Assess this cell for malaria.
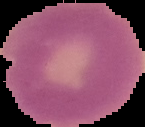
It is uninfected.

Image is 145×127 pixels. Segmented cell region on a black background. From a thin blood smear.